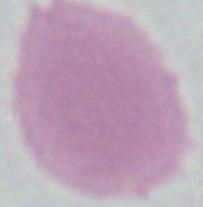 Captured at 1000x magnification. Photomicrograph. An erythrocyte is seen.